Locate every malaria parasite and every leukocyte.
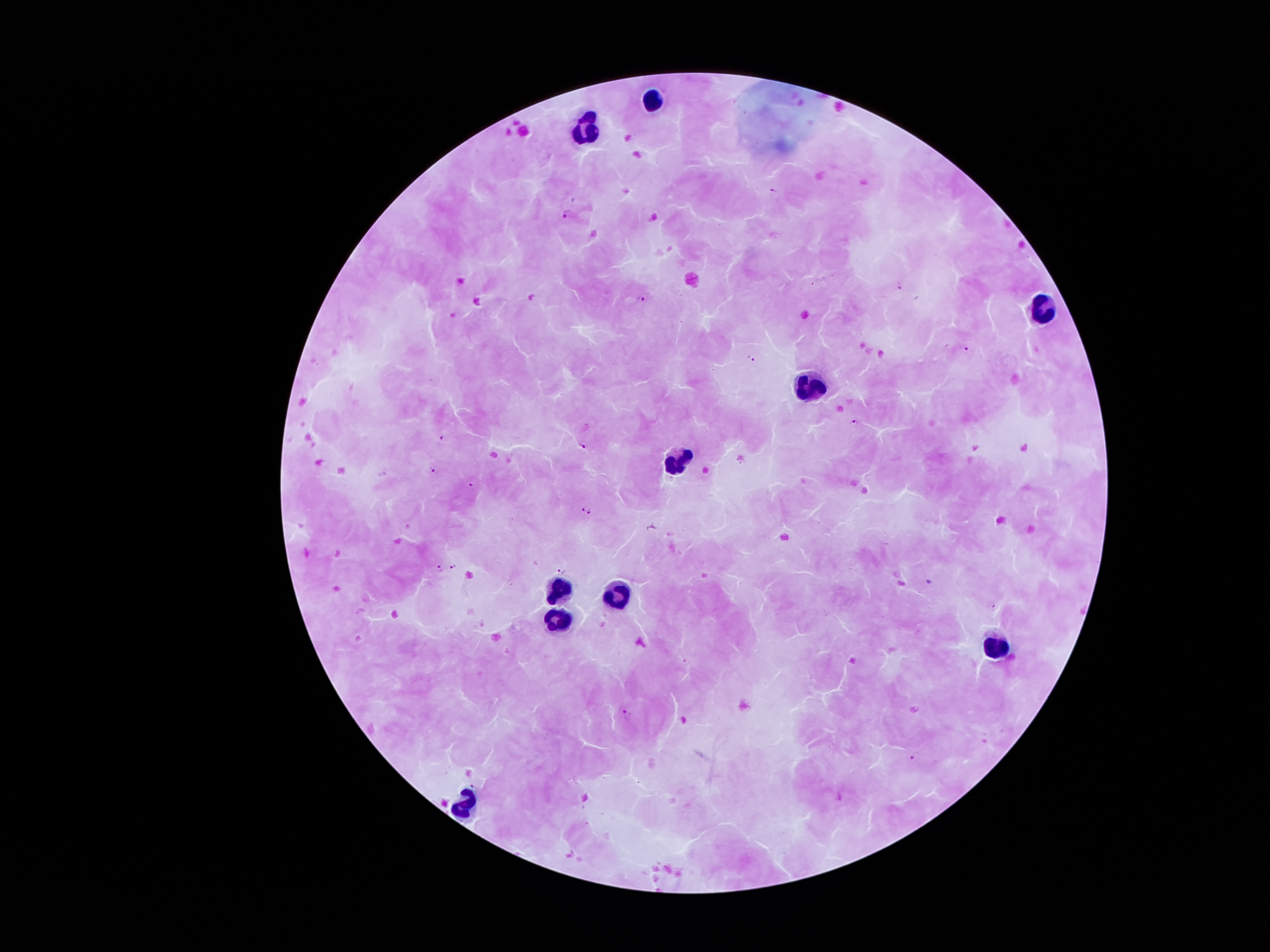
Approximate object centers, in pixels from the top-left corner.
Malaria parasites: (x=774, y=192), (x=566, y=214), (x=642, y=300), (x=966, y=349), (x=751, y=358), (x=854, y=423), (x=440, y=438), (x=584, y=447), (x=433, y=470), (x=472, y=485), (x=582, y=507), (x=590, y=513), (x=455, y=566), (x=440, y=569), (x=563, y=571), (x=627, y=713), (x=915, y=758).
Leukocytes: (x=656, y=99), (x=588, y=132), (x=1044, y=311), (x=808, y=382), (x=675, y=461), (x=555, y=587), (x=621, y=588), (x=559, y=618), (x=996, y=648), (x=458, y=801).

Image is 1270×952 pixels. Giemsa stain. Patient malaria status: positive for Plasmodium falciparum. Thick blood film. Photographed through the microscope eyepiece with a smartphone camera. 100x magnification. One field from this slide.